Assess this cell for malaria.
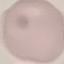
It is uninfected.

image type = cell patch, automatically extracted from a larger field of view and resized to 64 × 64 pixels
capture = smartphone camera at the microscope eyepiece
stain = Giemsa
preparation = thin smear